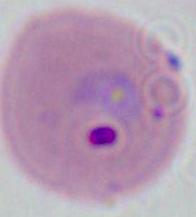
Summary:
  - Magnification: 400x or 1000x
  - Modality: photomicrograph
  - Identification: Plasmodium